Give the position of every leukocyte visible.
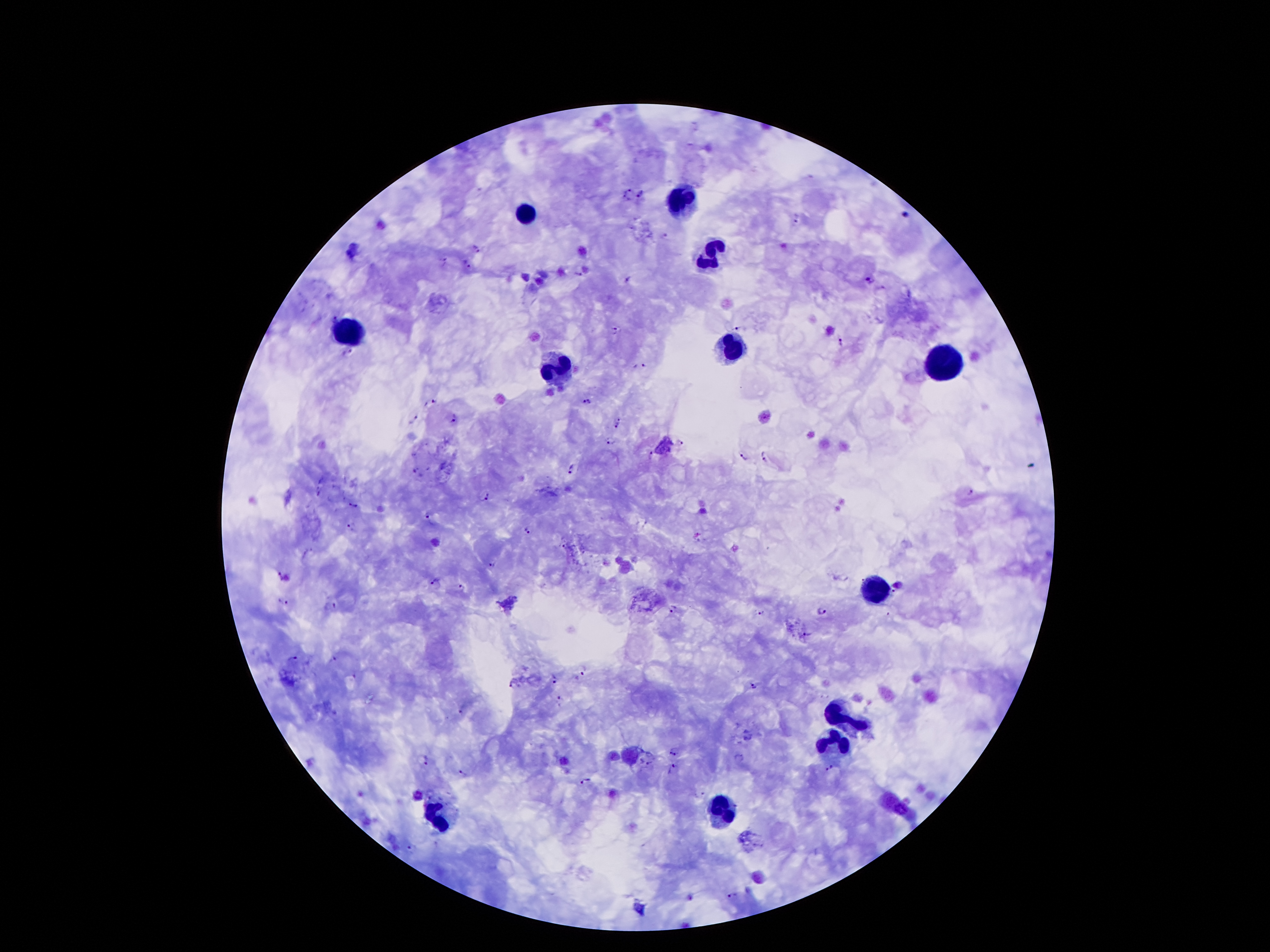
Approximate object centers, in pixels from the top-left corner.
Leukocytes: (x=678, y=202), (x=525, y=213), (x=716, y=257), (x=348, y=327), (x=731, y=353), (x=942, y=361), (x=554, y=367), (x=873, y=590), (x=844, y=715), (x=838, y=747), (x=725, y=810), (x=438, y=819).

preparation: thick blood smear
field_of_view: single
plasmodium_parasite_locations: 'approximate object centers, in pixels from the top-left corner: (x=641, y=192), (x=624, y=196), (x=905, y=215), (x=798, y=218), (x=666, y=235), (x=477, y=248), (x=443, y=260), (x=466, y=264), (x=578, y=273), (x=630, y=277), (x=868, y=278), (x=332, y=315), (x=737, y=326), (x=616, y=329), (x=842, y=342), (x=346, y=352), (x=638, y=366), (x=586, y=400), (x=429, y=403), (x=454, y=418), (x=414, y=419), (x=620, y=423), (x=609, y=442), (x=679, y=443), (x=742, y=454), (x=649, y=455), (x=764, y=455), (x=572, y=469), (x=416, y=472), (x=969, y=493), (x=485, y=495), (x=354, y=505), (x=427, y=517), (x=351, y=528), (x=526, y=530), (x=563, y=546), (x=491, y=567), (x=284, y=577), (x=436, y=583), (x=899, y=584), (x=462, y=587), (x=892, y=593), (x=283, y=601), (x=330, y=605), (x=675, y=608), (x=760, y=613), (x=820, y=613), (x=809, y=633), (x=292, y=657), (x=336, y=657), (x=582, y=669), (x=554, y=679), (x=513, y=684), (x=755, y=687), (x=559, y=697), (x=462, y=710), (x=675, y=753), (x=738, y=756), (x=425, y=760), (x=649, y=762), (x=674, y=767), (x=828, y=768), (x=463, y=774), (x=587, y=780), (x=701, y=794), (x=413, y=847), (x=733, y=895)'
capture: smartphone camera through the microscope eyepiece
stain: Giemsa
patient_malaria_status: positive for Plasmodium falciparum
image_size: 1270×952 pixels
magnification: 100x